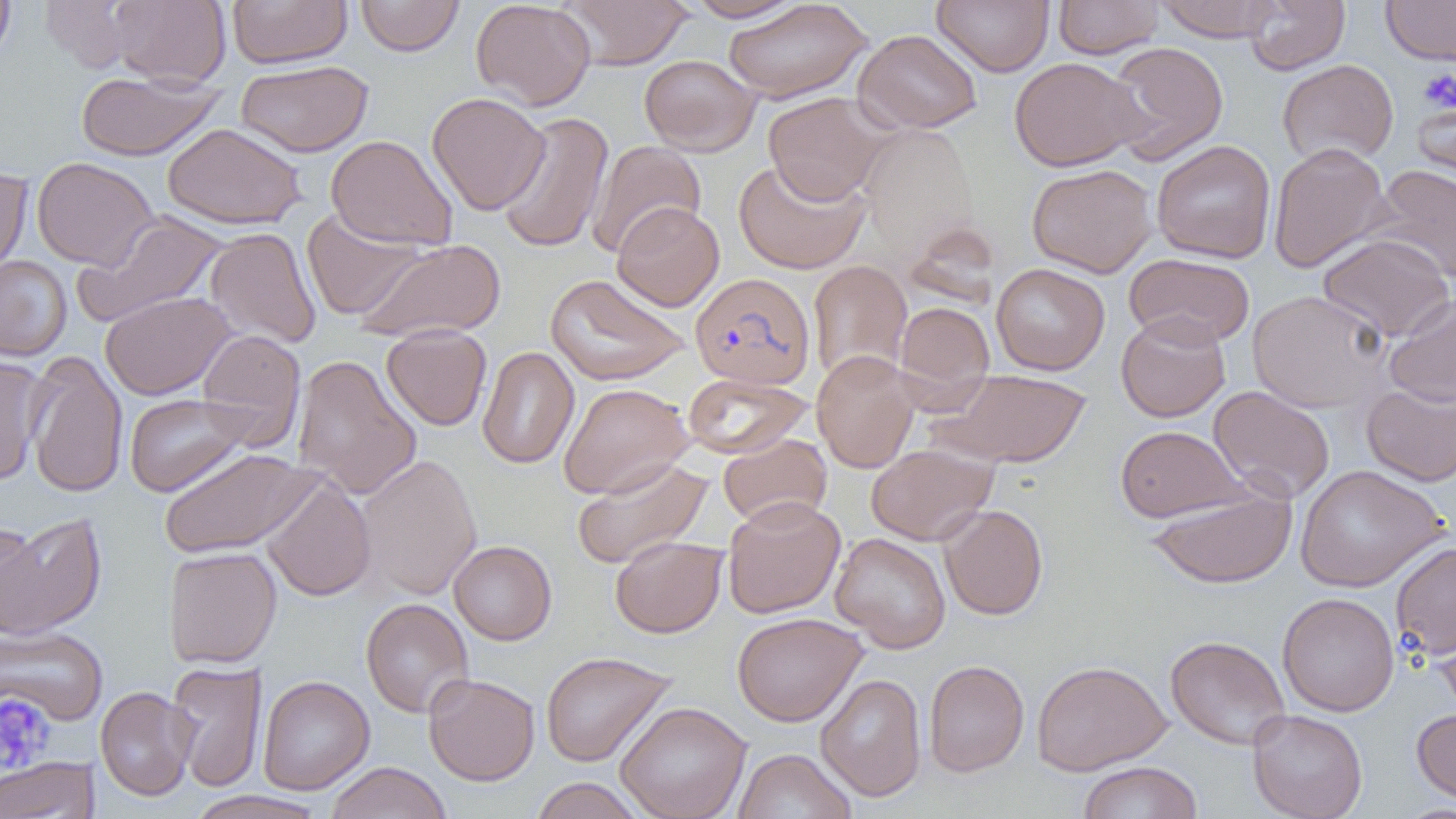

Summary:
  - Coordinate format: approximate bounding boxes as (x1,y1)-(x2,y2) corner pairs in pixels
  - Uninfected red blood cell locations: (0,0)-(17,65), (38,0)-(138,73), (107,0)-(231,87), (227,0)-(352,68), (355,0)-(464,57), (470,0)-(596,111), (558,0)-(692,69), (685,0)-(805,22), (932,0)-(1054,76), (1052,0)-(1164,59), (1153,0)-(1283,41), (1243,0)-(1349,75), (1381,0)-(1456,66), (722,1)-(872,102), (853,29)-(982,133), (1103,41)-(1229,165), (639,54)-(761,156), (1009,56)-(1146,171), (1277,59)-(1399,167), (235,60)-(374,157), (76,71)-(223,161), (427,92)-(550,215), (763,92)-(891,205), (1412,92)-(1456,196), (494,111)-(613,254), (162,122)-(307,231), (325,134)-(458,251), (587,140)-(706,258), (1151,140)-(1276,263), (1268,142)-(1392,272), (31,157)-(158,270), (733,158)-(870,274), (1026,163)-(1157,277), (1369,164)-(1456,284), (0,166)-(34,281), (612,202)-(725,311), (301,209)-(426,321), (73,213)-(227,327), (204,228)-(321,349), (1317,233)-(1455,342), (357,239)-(506,341), (1124,253)-(1255,347), (0,256)-(72,361), (807,260)-(912,385), (991,262)-(1110,375), (545,273)-(691,386), (1247,290)-(1391,412), (100,291)-(236,400), (1383,293)-(1456,408), (894,301)-(994,404), (1116,312)-(1231,422), (381,324)-(492,431), (196,329)-(306,448), (477,347)-(579,470), (24,349)-(129,499), (811,350)-(921,473), (0,353)-(48,486), (292,355)-(422,500), (931,368)-(1091,468), (682,373)-(814,459), (1361,381)-(1456,487), (558,382)-(694,499), (1208,385)-(1335,503), (124,393)-(254,497), (1114,425)-(1248,522), (717,433)-(832,528), (866,443)-(998,545), (157,447)-(321,559), (355,454)-(483,600), (571,457)-(714,570), (1295,465)-(1447,592), (261,476)-(376,601), (1145,484)-(1296,590), (722,496)-(845,618), (938,504)-(1048,620), (1,513)-(107,639), (1,518)-(42,637), (830,532)-(951,653), (609,535)-(727,638), (448,540)-(557,645), (1390,540)-(1456,660), (164,546)-(282,669), (1277,592)-(1399,716), (360,598)-(474,718), (732,612)-(867,726), (1432,615)-(1456,718), (0,625)-(109,726), (1165,635)-(1291,750), (540,650)-(677,767), (923,659)-(1029,777), (1032,659)-(1172,775), (166,660)-(267,792), (423,673)-(539,786), (815,673)-(927,801), (257,675)-(375,795), (95,686)-(198,801), (615,701)-(752,819), (1411,706)-(1456,806), (1247,708)-(1368,819), (733,748)-(856,819), (0,756)-(98,818), (1077,761)-(1202,819), (325,762)-(452,819), (529,777)-(644,818), (184,790)-(329,819)
  - Plasmodium falciparum-infected red blood cell locations: (690,272)-(815,390)
  - Platelet locations: (1417,68)-(1456,114), (0,694)-(54,773)
  - Slide-level diagnosis: Plasmodium falciparum
  - Magnification: 1000x
  - Image size: 1456×819 pixels
  - Modality: light microscopy
  - Field of view: single
  - Preparation: thin blood smear